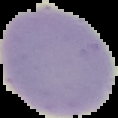

Image is 118×118 pixels. Result: no Plasmodium parasites detected. Segmented cell region on a black background. From a thin blood film.